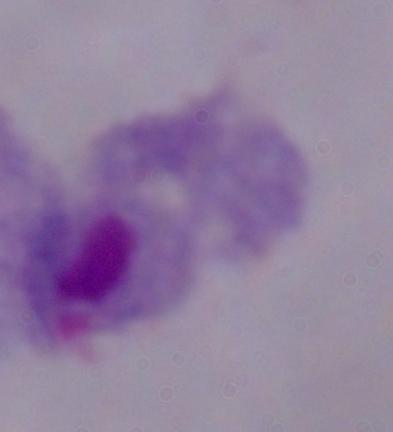

Micrograph. A trichomonad is seen. 1000x magnification.